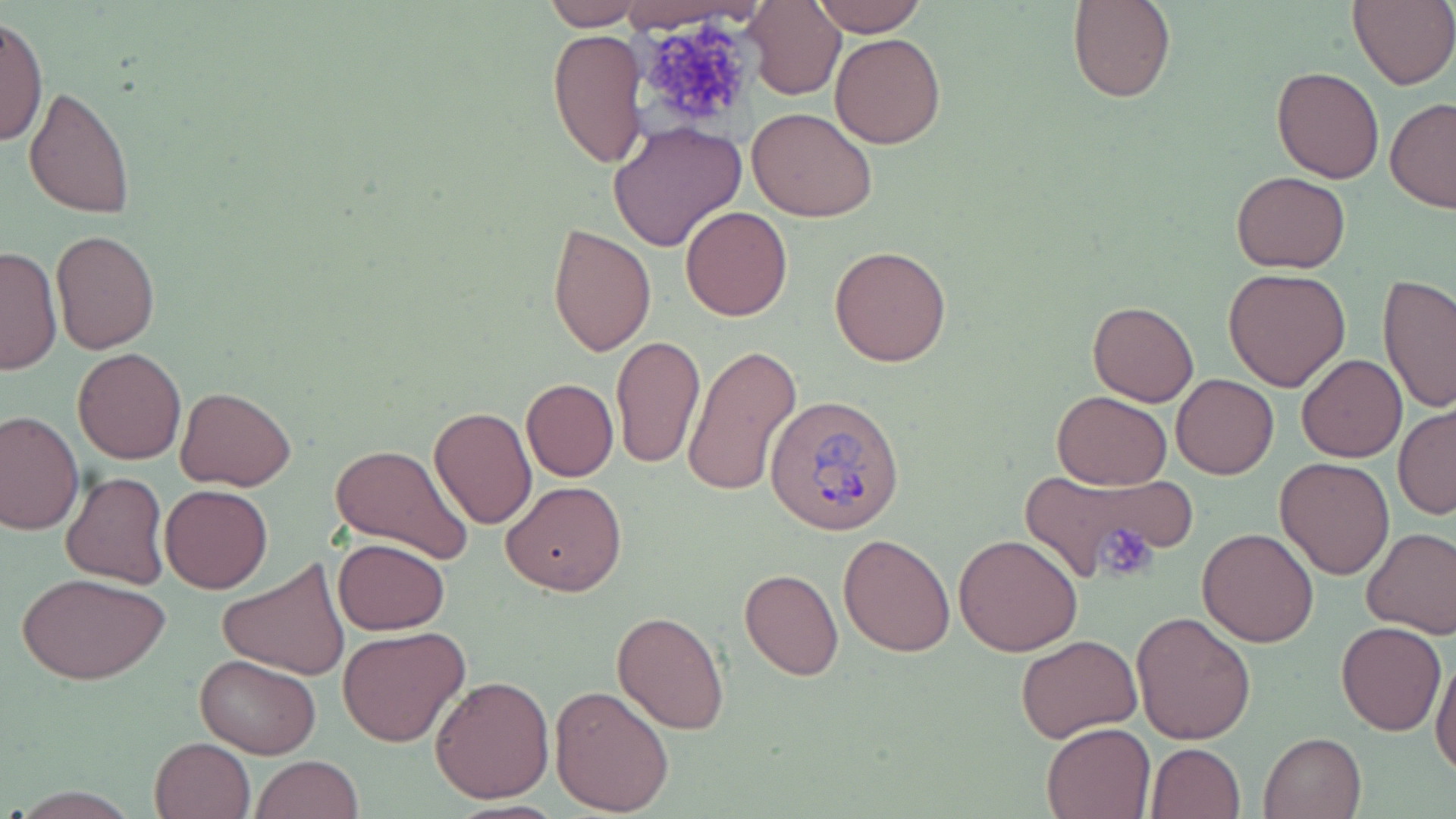
Approximate bounding boxes as (x1,y1)-(x2,y2) corner pairs in pixels. Platelet locations: (636,18)-(762,136), (1094,521)-(1156,579). Uninfected red blood cell locations: (611,0)-(763,33), (810,0)-(927,35), (1067,0)-(1175,103), (745,1)-(845,100), (1347,1)-(1456,89), (537,2)-(641,30), (1,14)-(48,148), (546,27)-(645,170), (831,33)-(946,148), (1271,66)-(1385,183), (24,84)-(137,218), (1384,98)-(1456,214), (748,107)-(877,222), (608,120)-(747,252), (1230,171)-(1351,273), (680,206)-(793,321), (545,223)-(657,358), (50,229)-(160,354), (829,243)-(954,367), (1,244)-(60,378), (1222,267)-(1351,392), (1378,274)-(1455,413), (1086,298)-(1200,406), (610,334)-(705,468), (681,342)-(802,499), (72,348)-(186,464), (1297,355)-(1407,462), (1171,374)-(1278,479), (520,378)-(618,482), (176,387)-(297,491), (1052,390)-(1172,490), (1393,402)-(1456,520), (428,407)-(537,530), (0,410)-(83,536), (329,443)-(474,566), (1275,457)-(1395,579), (1016,465)-(1184,585), (60,470)-(170,590), (502,480)-(627,596), (160,484)-(273,594), (1361,526)-(1456,639), (1197,528)-(1319,647), (953,532)-(1085,657), (838,534)-(955,656), (330,537)-(450,634), (216,557)-(351,679), (739,568)-(843,681), (17,572)-(172,684), (611,608)-(730,735), (1131,611)-(1257,743), (1336,622)-(1446,736), (338,625)-(471,747), (1016,635)-(1142,744), (195,653)-(322,758), (1431,655)-(1456,778), (431,675)-(554,803), (549,683)-(675,815), (1041,721)-(1157,818), (1259,731)-(1367,819), (149,736)-(255,819), (1146,743)-(1246,818), (250,754)-(363,819). Plasmodium ovale-infected red blood cell locations: (764,392)-(907,534). Slide-level diagnosis: Plasmodium ovale. Light microscopy. Single field of view. Image is 1456×819 pixels. May-Grünwald-Giemsa stain. Captured at 1000x magnification. Thin blood smear.